Locate every blood parasite and identify its species.
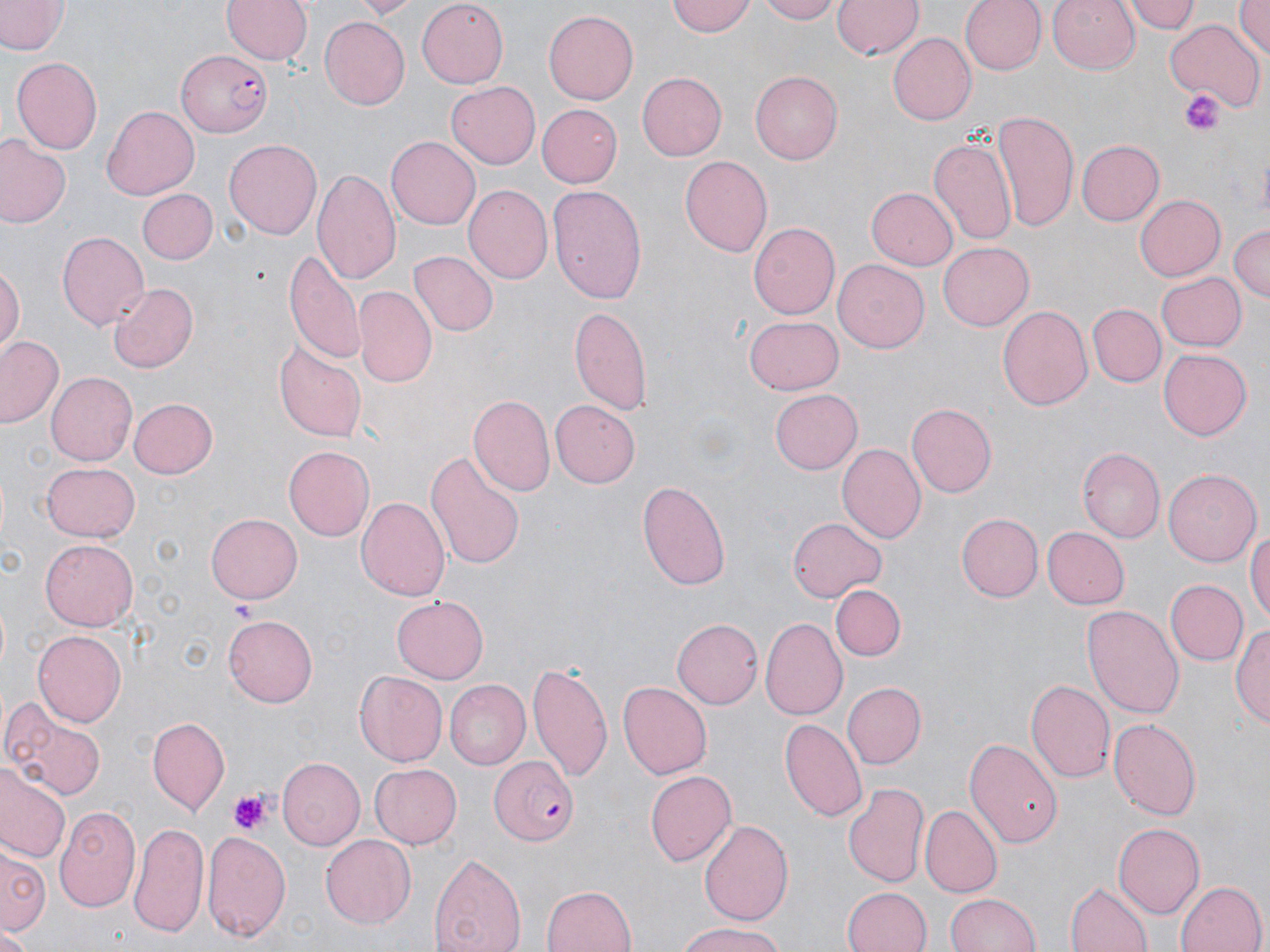
Approximate bounding boxes as named x1/y1/x2/y2 corners in pixels.
Plasmodium falciparum-infected red blood cells: (x1=177, y1=52, x2=274, y2=137), (x1=487, y1=756, x2=578, y2=847).
No Plasmodium ovale, Plasmodium malariae, Plasmodium vivax, Babesia divergens, or Trypanosoma brucei observed.

slide-level diagnosis = Plasmodium falciparum
stain = May-Grünwald-Giemsa
platelet locations = approximate bounding boxes as named x1/y1/x2/y2 corners in pixels: (x1=1179, y1=89, x2=1227, y2=137), (x1=227, y1=596, x2=254, y2=622), (x1=228, y1=793, x2=272, y2=837)
modality = optical microscopy
magnification = 1000x
field of view = single
uninfected red blood cell locations = approximate bounding boxes as named x1/y1/x2/y2 corners in pixels: (x1=222, y1=0, x2=312, y2=66), (x1=350, y1=0, x2=421, y2=18), (x1=416, y1=0, x2=509, y2=88), (x1=669, y1=0, x2=758, y2=37), (x1=758, y1=0, x2=842, y2=24), (x1=832, y1=0, x2=922, y2=61), (x1=962, y1=0, x2=1043, y2=76), (x1=1046, y1=0, x2=1141, y2=75), (x1=1126, y1=0, x2=1200, y2=33), (x1=1232, y1=0, x2=1270, y2=59), (x1=0, y1=1, x2=66, y2=56), (x1=544, y1=9, x2=639, y2=104), (x1=319, y1=18, x2=410, y2=109), (x1=1166, y1=20, x2=1264, y2=109), (x1=887, y1=33, x2=974, y2=125), (x1=10, y1=56, x2=103, y2=157), (x1=638, y1=70, x2=726, y2=161), (x1=752, y1=70, x2=847, y2=165), (x1=446, y1=82, x2=541, y2=170), (x1=536, y1=104, x2=621, y2=187), (x1=102, y1=105, x2=199, y2=200), (x1=993, y1=109, x2=1079, y2=231), (x1=0, y1=135, x2=71, y2=229), (x1=387, y1=136, x2=480, y2=229), (x1=929, y1=136, x2=1016, y2=246), (x1=224, y1=139, x2=323, y2=240), (x1=1075, y1=139, x2=1163, y2=226), (x1=679, y1=156, x2=773, y2=258), (x1=313, y1=166, x2=403, y2=287), (x1=463, y1=183, x2=551, y2=284), (x1=547, y1=186, x2=647, y2=302), (x1=867, y1=187, x2=958, y2=270), (x1=139, y1=190, x2=217, y2=264), (x1=1135, y1=193, x2=1225, y2=279), (x1=749, y1=221, x2=840, y2=319), (x1=1227, y1=224, x2=1269, y2=305), (x1=57, y1=232, x2=149, y2=331), (x1=939, y1=244, x2=1034, y2=333), (x1=285, y1=245, x2=366, y2=368), (x1=407, y1=250, x2=498, y2=337), (x1=834, y1=258, x2=929, y2=354), (x1=0, y1=265, x2=22, y2=357), (x1=1154, y1=271, x2=1245, y2=350), (x1=107, y1=281, x2=198, y2=374), (x1=353, y1=286, x2=436, y2=386), (x1=569, y1=302, x2=655, y2=419), (x1=997, y1=304, x2=1094, y2=412), (x1=1088, y1=304, x2=1164, y2=387), (x1=743, y1=316, x2=843, y2=394), (x1=1, y1=338, x2=62, y2=430), (x1=274, y1=342, x2=366, y2=443), (x1=1158, y1=349, x2=1252, y2=439), (x1=47, y1=371, x2=136, y2=464), (x1=770, y1=389, x2=862, y2=475), (x1=469, y1=396, x2=555, y2=495), (x1=126, y1=397, x2=218, y2=480), (x1=550, y1=399, x2=641, y2=487), (x1=907, y1=402, x2=999, y2=497), (x1=836, y1=442, x2=925, y2=543), (x1=283, y1=446, x2=375, y2=540), (x1=1075, y1=447, x2=1163, y2=544), (x1=424, y1=450, x2=527, y2=568), (x1=40, y1=461, x2=139, y2=541), (x1=1164, y1=467, x2=1261, y2=569), (x1=637, y1=479, x2=730, y2=590), (x1=356, y1=495, x2=451, y2=604), (x1=957, y1=513, x2=1042, y2=601), (x1=206, y1=514, x2=303, y2=604), (x1=789, y1=515, x2=886, y2=602), (x1=1246, y1=525, x2=1270, y2=628), (x1=1042, y1=527, x2=1129, y2=609), (x1=40, y1=535, x2=138, y2=628), (x1=1167, y1=580, x2=1247, y2=666), (x1=832, y1=585, x2=904, y2=662), (x1=392, y1=596, x2=488, y2=683), (x1=1084, y1=604, x2=1183, y2=720), (x1=225, y1=613, x2=318, y2=706), (x1=761, y1=617, x2=848, y2=719), (x1=673, y1=618, x2=763, y2=708), (x1=1234, y1=618, x2=1269, y2=732), (x1=33, y1=630, x2=126, y2=726), (x1=526, y1=661, x2=613, y2=781), (x1=354, y1=669, x2=448, y2=766), (x1=1025, y1=677, x2=1115, y2=783), (x1=616, y1=679, x2=713, y2=780), (x1=444, y1=680, x2=530, y2=767), (x1=840, y1=682, x2=925, y2=770), (x1=0, y1=698, x2=111, y2=803), (x1=1108, y1=715, x2=1201, y2=822), (x1=148, y1=717, x2=229, y2=813), (x1=780, y1=718, x2=868, y2=821), (x1=965, y1=737, x2=1062, y2=850), (x1=277, y1=756, x2=365, y2=850), (x1=0, y1=763, x2=71, y2=866), (x1=370, y1=763, x2=463, y2=849), (x1=643, y1=768, x2=736, y2=868), (x1=842, y1=781, x2=931, y2=891), (x1=53, y1=805, x2=141, y2=913), (x1=919, y1=806, x2=1002, y2=899), (x1=698, y1=818, x2=794, y2=924), (x1=129, y1=819, x2=211, y2=940), (x1=1113, y1=824, x2=1204, y2=916), (x1=202, y1=831, x2=291, y2=943), (x1=320, y1=834, x2=414, y2=929), (x1=0, y1=844, x2=49, y2=941), (x1=428, y1=848, x2=527, y2=952), (x1=1175, y1=878, x2=1267, y2=952), (x1=1066, y1=881, x2=1155, y2=952), (x1=541, y1=883, x2=638, y2=952), (x1=841, y1=885, x2=932, y2=952), (x1=944, y1=891, x2=1043, y2=951), (x1=676, y1=921, x2=788, y2=952), (x1=0, y1=930, x2=33, y2=952)
image size = 1270×952 pixels
preparation = thin blood smear